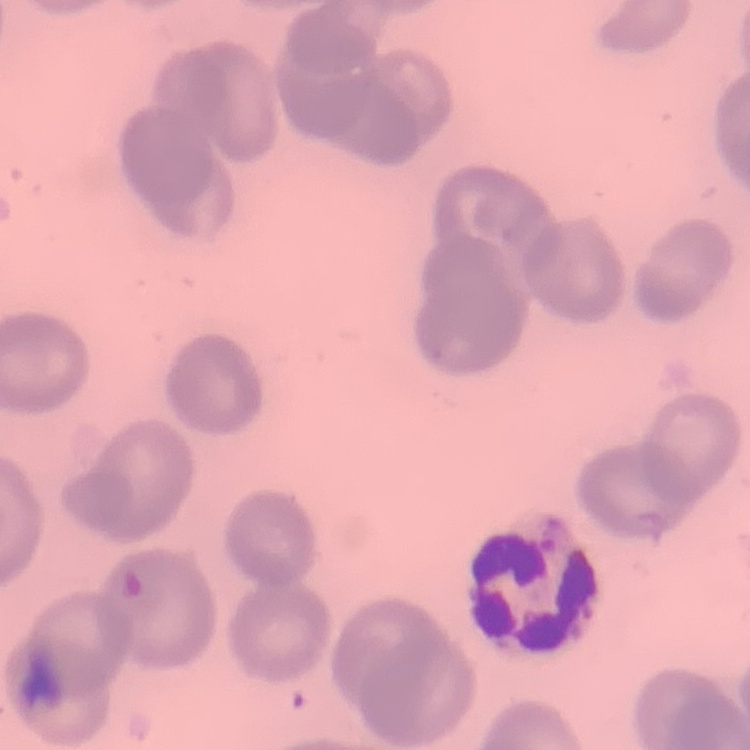
Summary:
  - Erythrocyte morphology: no rouleaux formation
  - Preparation: thin blood film
  - Image type: square crop of a larger photomicrograph
  - Stain: Field's or Giemsa